Assess this cell for malaria.
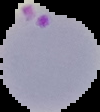

It is parasitized.

Summary:
  - Preparation: thin blood smear
  - Image size: 100×112 pixels
  - Image type: cell region segmented out of the field of view; surrounding area masked to black